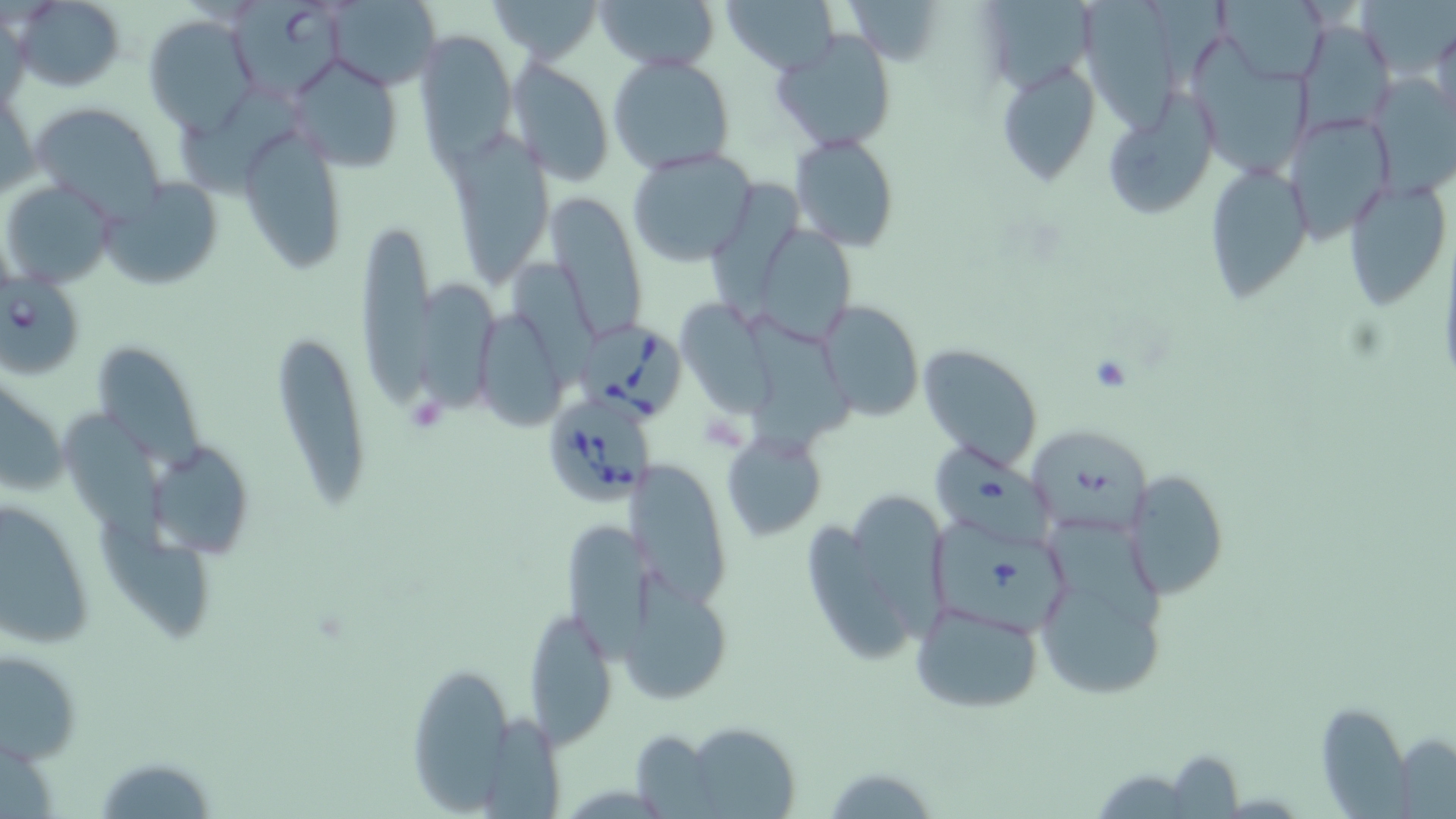
slide_level_diagnosis: Babesia divergens
image_size: 1456×819 pixels
modality: optical microscopy
uninfected_red_blood_cell_locations: 'approximate bounding boxes as (x1, y1, x2, y2) in pixels: (12, 0, 125, 90), (485, 0, 603, 64), (593, 0, 720, 72), (720, 0, 838, 74), (850, 0, 944, 63), (1078, 0, 1180, 141), (1215, 0, 1331, 81), (1357, 0, 1456, 81), (320, 1, 442, 90), (985, 1, 1094, 97), (141, 14, 258, 133), (1296, 18, 1396, 136), (1431, 19, 1456, 137), (412, 29, 516, 166), (771, 30, 897, 152), (1189, 37, 1316, 179), (288, 53, 402, 170), (607, 54, 735, 174), (508, 58, 615, 183), (993, 60, 1102, 191), (1, 82, 37, 201), (178, 88, 297, 203), (1108, 100, 1213, 220), (32, 102, 166, 218), (1284, 113, 1396, 241), (237, 121, 350, 273), (789, 133, 898, 253), (446, 136, 552, 285), (626, 146, 760, 266), (1205, 161, 1314, 305), (1341, 175, 1451, 312), (3, 178, 116, 287), (104, 178, 227, 292), (708, 179, 805, 317), (545, 193, 646, 344), (356, 208, 439, 425), (761, 230, 858, 347), (513, 266, 604, 393), (411, 277, 500, 419), (814, 300, 925, 421), (678, 302, 775, 421), (738, 310, 862, 462), (480, 318, 570, 425), (266, 327, 372, 513), (918, 342, 1045, 470), (93, 348, 210, 478), (1, 371, 69, 499), (60, 410, 168, 540), (1025, 422, 1154, 537), (721, 431, 825, 543), (151, 449, 254, 562), (930, 449, 1064, 555), (634, 468, 740, 610), (1124, 470, 1229, 599), (858, 495, 952, 643), (0, 496, 97, 648), (1034, 518, 1174, 704), (93, 520, 217, 643), (810, 520, 913, 667), (567, 522, 657, 660), (934, 523, 1079, 638), (629, 578, 733, 703), (909, 600, 1045, 715), (524, 616, 619, 749), (2, 646, 83, 766), (407, 658, 519, 813), (1316, 703, 1413, 815), (484, 713, 564, 816), (683, 724, 801, 819), (630, 731, 722, 817), (1393, 735, 1456, 818), (1165, 750, 1245, 817), (93, 757, 222, 817), (820, 764, 942, 818)'
babesia_divergens_infected_red_blood_cell_locations: 'approximate bounding boxes as (x1, y1, x2, y2) in pixels: (233, 1, 351, 98), (2, 271, 88, 383), (578, 322, 685, 424), (541, 395, 657, 509)'
preparation: thin blood film
magnification: 1000x
stain: May-Grünwald-Giemsa
field_of_view: one of a larger specimen